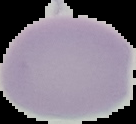

Summary:
  - Image type: segmented cell region with the area outside set to black
  - Malaria status: uninfected
  - Preparation: thin blood smear
  - Image size: 136×124 pixels